Report the malaria status of this cell.
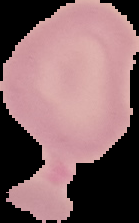
It is uninfected.

image_size: 139×223 pixels
image_type: segmented cell region with the area outside set to black
preparation: thin blood film